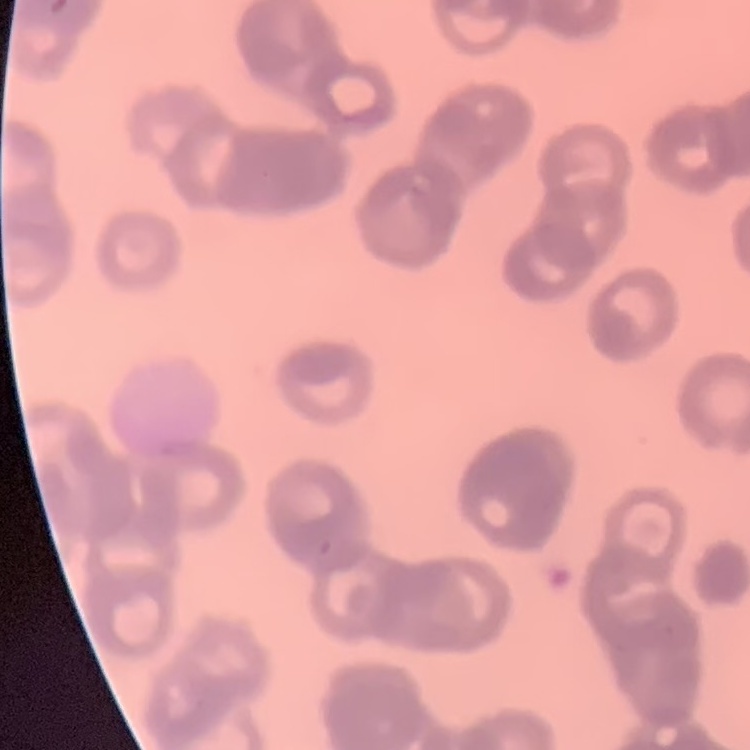
{
  "red_blood_cell_morphology": "rouleaux formation",
  "stain": "Field's or Giemsa",
  "preparation": "thin blood smear",
  "image_type": "one tile cut from a larger photomicrograph"
}